Point out each Plasmodium parasite.
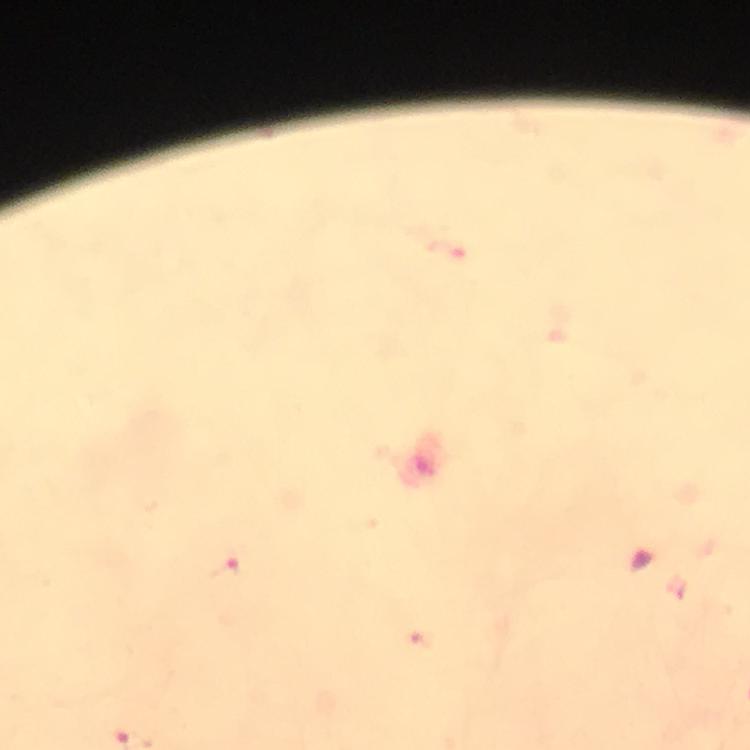

Approximate centers as {x, y} in pixels.
Plasmodium parasites: {446, 251}, {225, 569}.

Summary:
  - Image size: 750×750 pixels
  - Context: from a malaria diagnostic workup
  - Magnification: 100x
  - Capture: smartphone photograph through a microscope
  - Preparation: thick smear
  - Cropped from: one field of view
  - Stain: Giemsa
  - Immersion oil: applied